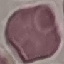

Malaria status: uninfected. Automatically extracted cell patch, resized to 64 × 64 pixels. Thin smear of blood. Giemsa stain. Acquired by smartphone through the microscope eyepiece.